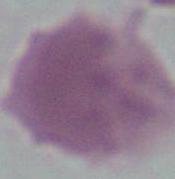
Summary:
  - Magnification: 1000x
  - Identification: erythrocyte
  - Modality: micrograph